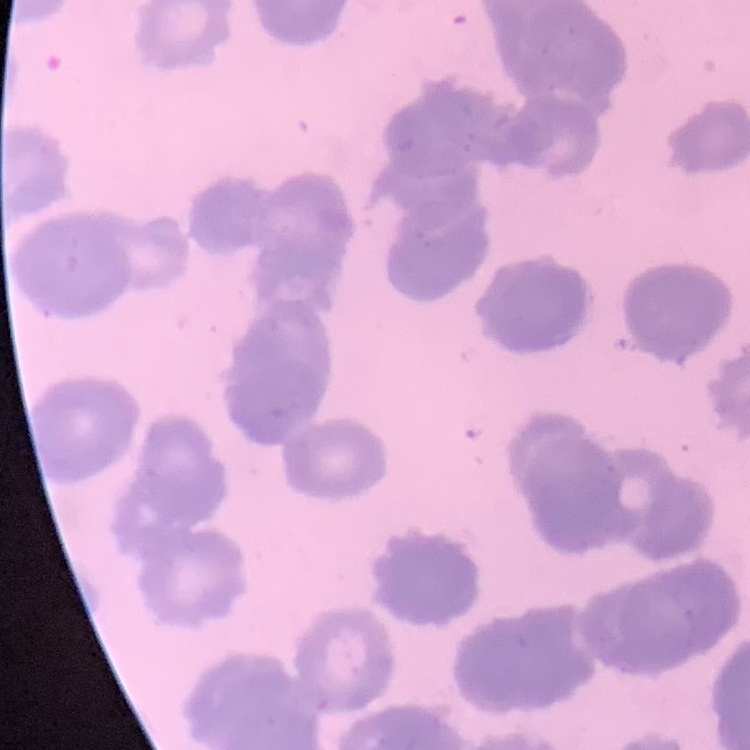
The erythrocytes exhibit rouleaux formation. One tile cut from a larger photomicrograph. Stained with either Field's or Giemsa. Thin blood film.